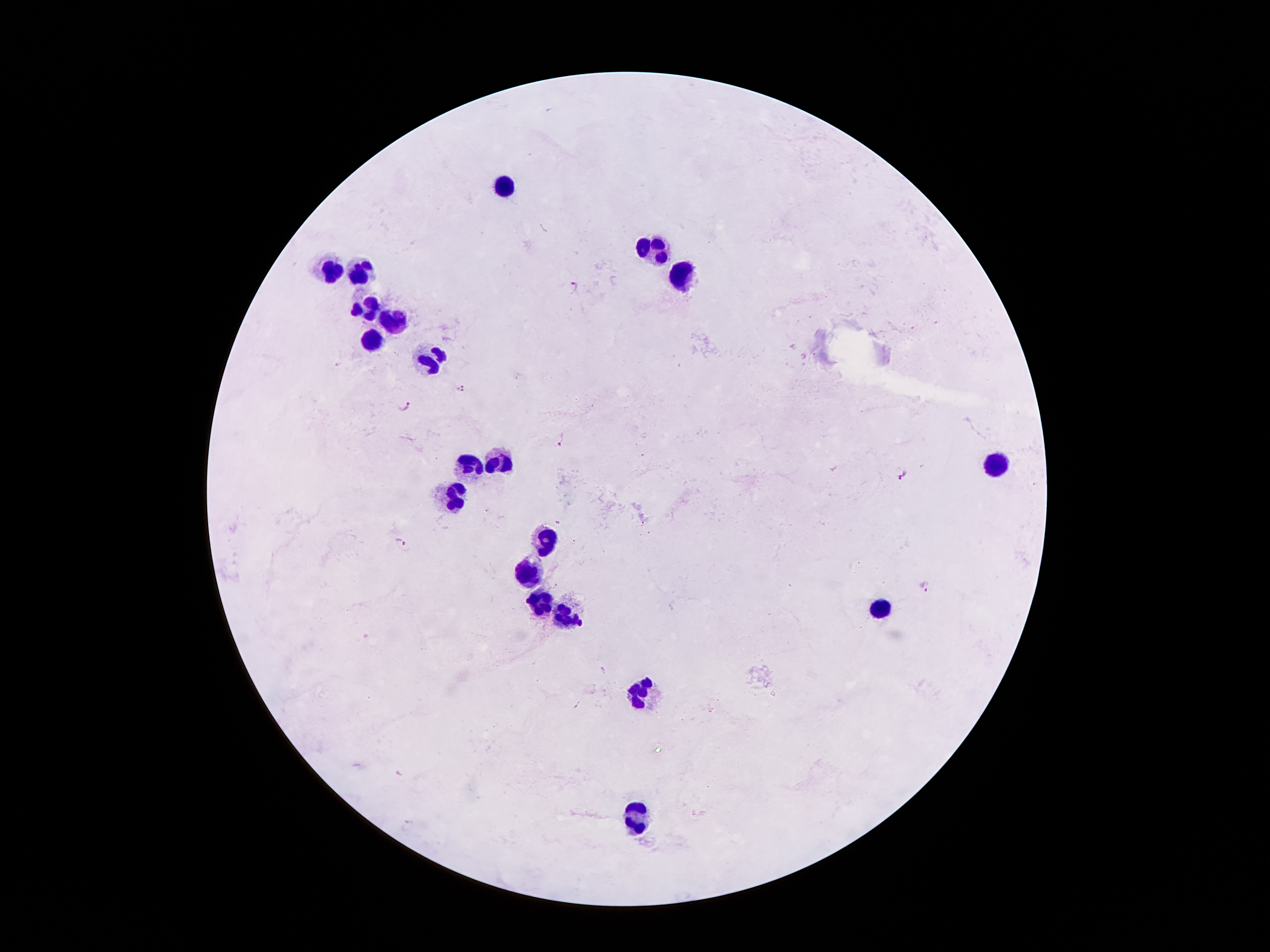
coordinate format = approximate object centers, in pixels from the top-left corner
Plasmodium parasite locations = (x=576, y=286), (x=461, y=388), (x=406, y=407), (x=562, y=440), (x=903, y=475), (x=401, y=542), (x=927, y=586)
leukocyte locations = (x=508, y=188), (x=655, y=250), (x=326, y=269), (x=357, y=270), (x=682, y=279), (x=363, y=307), (x=392, y=322), (x=371, y=343), (x=435, y=363), (x=496, y=461), (x=471, y=464), (x=995, y=464), (x=458, y=496), (x=546, y=540), (x=529, y=572), (x=537, y=600), (x=878, y=611), (x=565, y=617), (x=641, y=691), (x=638, y=818)
patient malaria status = infected with Plasmodium falciparum
image size = 1270×952 pixels
capture = smartphone through the microscope eyepiece
preparation = thick blood film
magnification = 100x
field of view = one from this slide
stain = Giemsa